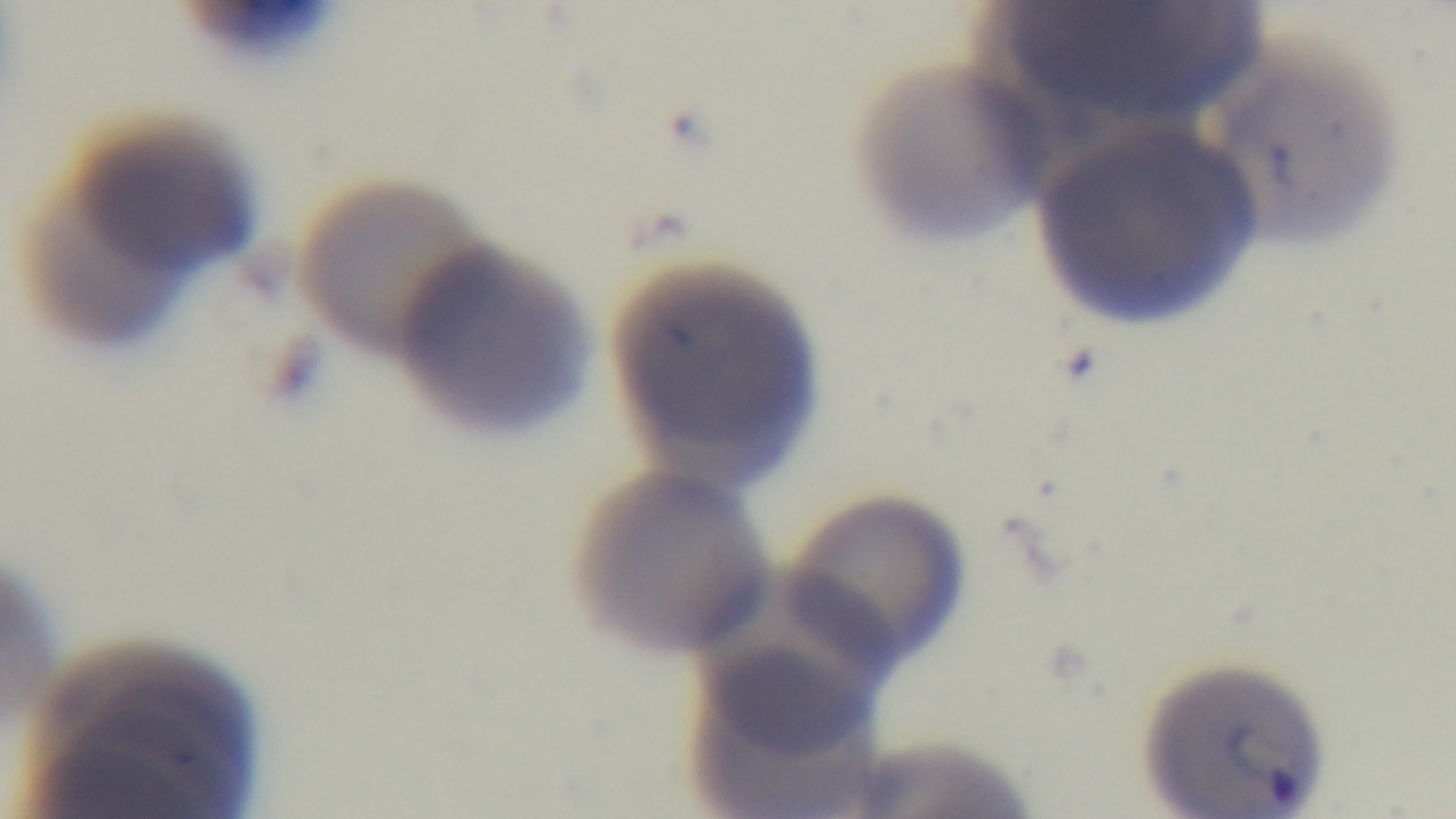
One field from the slide. Light microscopy. Oil-immersion objective, 100x. Malaria status: infected. Giemsa stain. Captured with a mounted 4K digital camera. Preparation: thin.